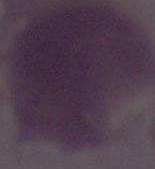

modality = micrograph
identification = red blood cell
magnification = 1000x